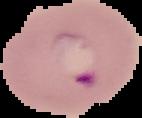 Malaria status: parasitized. The area outside the segmented cell region is set to black. From a thin blood smear. Image is 142×118 pixels.